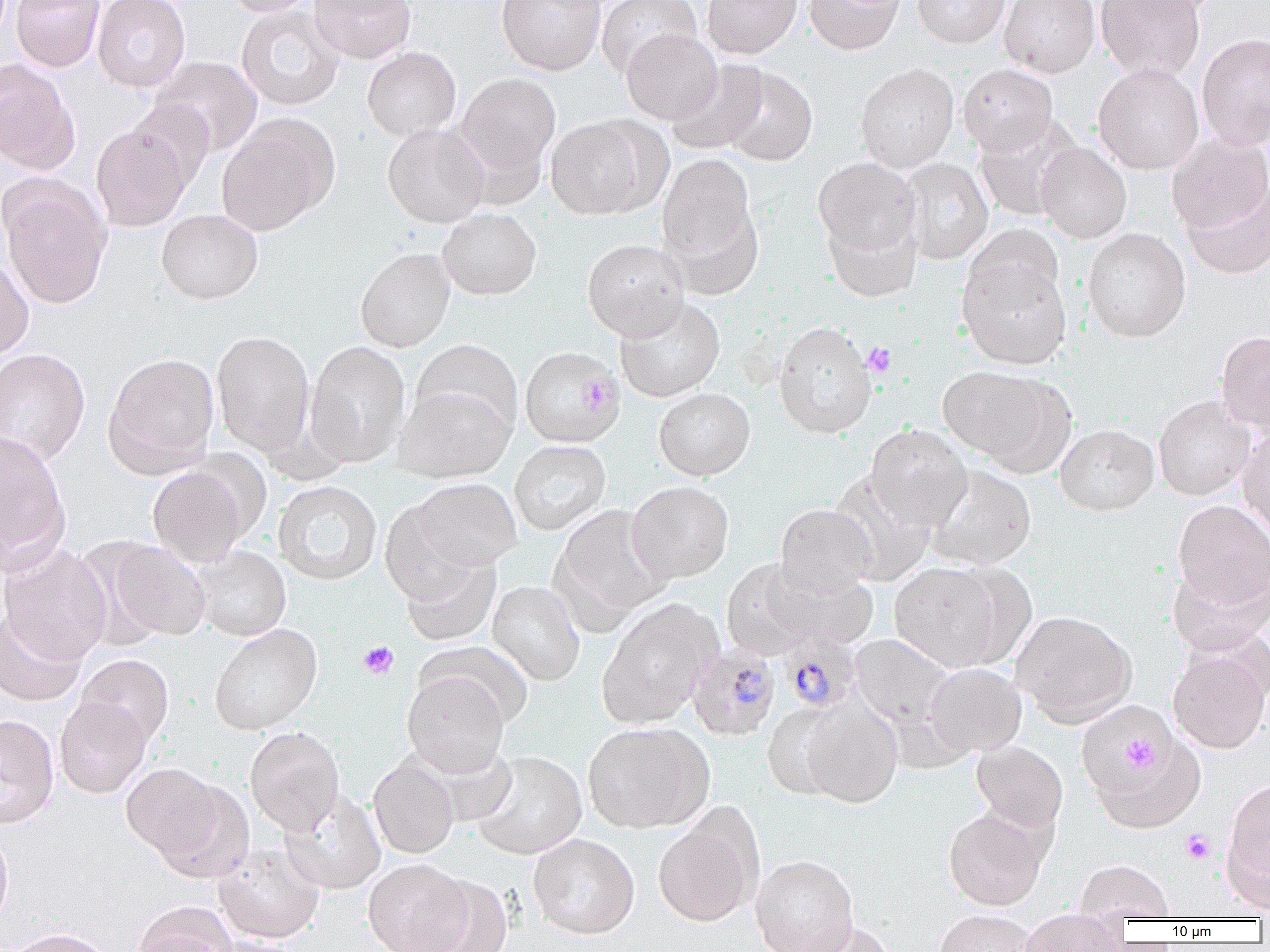
Approximate bounding boxes as (x1, y1, x2, y2) in pixels. Platelet locations: (862, 342, 896, 377), (358, 640, 399, 679), (1120, 732, 1158, 771), (1181, 829, 1216, 864). Uninfected red blood cell locations: (10, 0, 105, 72), (92, 0, 191, 92), (225, 0, 319, 17), (309, 0, 416, 64), (496, 0, 606, 76), (596, 0, 701, 79), (702, 0, 802, 59), (804, 0, 905, 55), (912, 0, 1009, 48), (999, 0, 1100, 79), (1096, 0, 1205, 82), (1117, 0, 1223, 18), (235, 4, 346, 112), (621, 29, 722, 124), (1196, 32, 1270, 151), (362, 47, 461, 141), (151, 57, 262, 156), (0, 60, 80, 174), (666, 60, 769, 156), (855, 63, 959, 173), (1093, 63, 1204, 175), (958, 64, 1058, 155), (721, 66, 817, 166), (456, 72, 561, 180), (125, 99, 215, 191), (216, 115, 338, 235), (973, 115, 1083, 221), (546, 116, 653, 220), (382, 123, 490, 227), (90, 124, 192, 231), (1166, 133, 1270, 236), (1036, 142, 1132, 244), (657, 154, 759, 269), (898, 157, 993, 265), (813, 158, 921, 258), (1, 181, 111, 310), (1180, 181, 1270, 279), (438, 208, 542, 300), (156, 209, 263, 304), (823, 212, 922, 303), (966, 224, 1063, 309), (1082, 229, 1191, 342), (582, 239, 689, 340), (355, 247, 456, 353), (0, 253, 34, 362), (957, 256, 1072, 370), (614, 297, 725, 402), (773, 321, 876, 438), (211, 331, 315, 457), (1216, 331, 1270, 436), (412, 339, 522, 437), (304, 341, 411, 468), (520, 346, 626, 448), (0, 348, 90, 465), (103, 353, 220, 476), (939, 366, 1072, 473), (394, 385, 516, 483), (654, 388, 755, 481), (1153, 395, 1256, 501), (1054, 423, 1159, 515), (865, 425, 972, 530), (1237, 426, 1270, 542), (0, 431, 69, 568), (509, 440, 611, 536), (923, 464, 1036, 570), (148, 466, 250, 568), (828, 470, 937, 585), (410, 478, 521, 572), (273, 481, 383, 586), (627, 481, 734, 583), (1173, 500, 1270, 612), (379, 502, 487, 608), (775, 504, 875, 596), (551, 505, 672, 627), (101, 539, 212, 643), (0, 544, 112, 665), (193, 547, 291, 641), (399, 551, 502, 647), (721, 559, 822, 660), (1167, 560, 1269, 656), (759, 562, 879, 651), (889, 562, 1007, 672), (487, 581, 585, 686), (597, 600, 723, 729), (0, 609, 87, 707), (1011, 610, 1137, 728), (209, 623, 322, 735), (850, 634, 958, 733), (1168, 648, 1270, 754), (75, 654, 173, 748), (925, 663, 1026, 758), (402, 671, 509, 777), (55, 696, 152, 798), (800, 696, 902, 807), (763, 704, 846, 800), (1078, 707, 1199, 824), (0, 715, 59, 828), (583, 722, 714, 833), (245, 727, 345, 836), (971, 741, 1068, 833), (471, 751, 587, 860), (368, 757, 459, 859), (121, 763, 229, 868), (1221, 775, 1270, 910), (153, 780, 254, 885), (279, 790, 386, 895), (943, 807, 1048, 910), (653, 813, 763, 928), (0, 826, 13, 929), (528, 833, 640, 939), (212, 844, 325, 944), (751, 854, 858, 952), (363, 859, 472, 952), (1074, 859, 1175, 920), (408, 875, 514, 952), (133, 903, 237, 952), (933, 911, 1042, 952), (1017, 913, 1128, 951), (790, 921, 898, 952), (2, 929, 116, 952), (198, 936, 299, 952). Plasmodium malariae-infected red blood cell locations: (778, 630, 862, 713), (685, 644, 781, 740). Slide-level diagnosis: Plasmodium malariae. Optical microscopy. One field of a larger specimen. Thin blood film. Image is 1270×952 pixels. 1000x magnification.